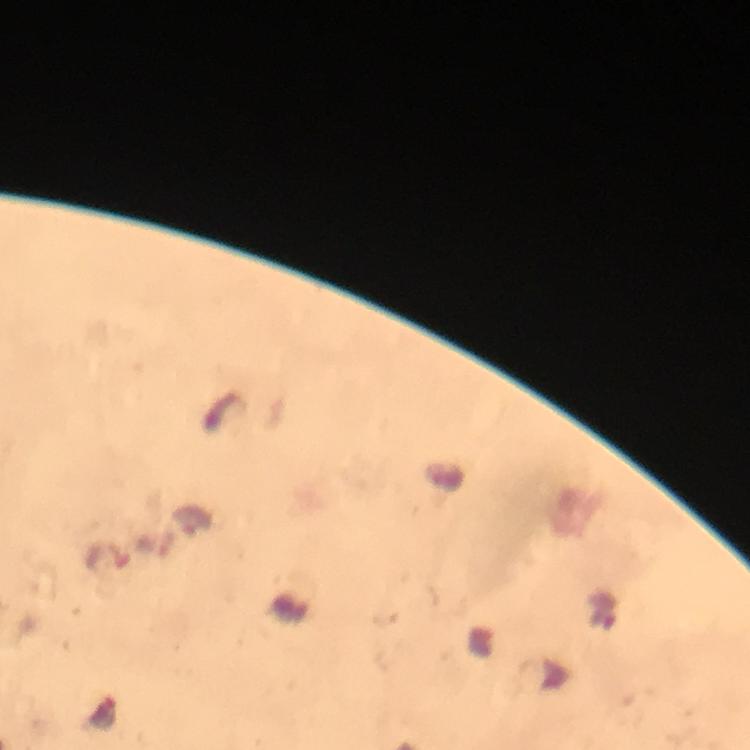 Approximate centers as (x, y) in pixels. Malaria parasite locations: (104, 714). From a malaria diagnostic workup. Image is 750×750 pixels. Cropped region of a single field of view. Immersion oil applied. Photographed through the microscope with a smartphone camera. Thick smear. Giemsa-stained preparation. 100x magnification.